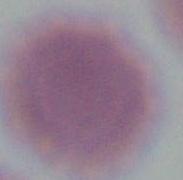

{
  "identification": "red blood cell",
  "modality": "photomicrograph",
  "magnification": "1000x"
}